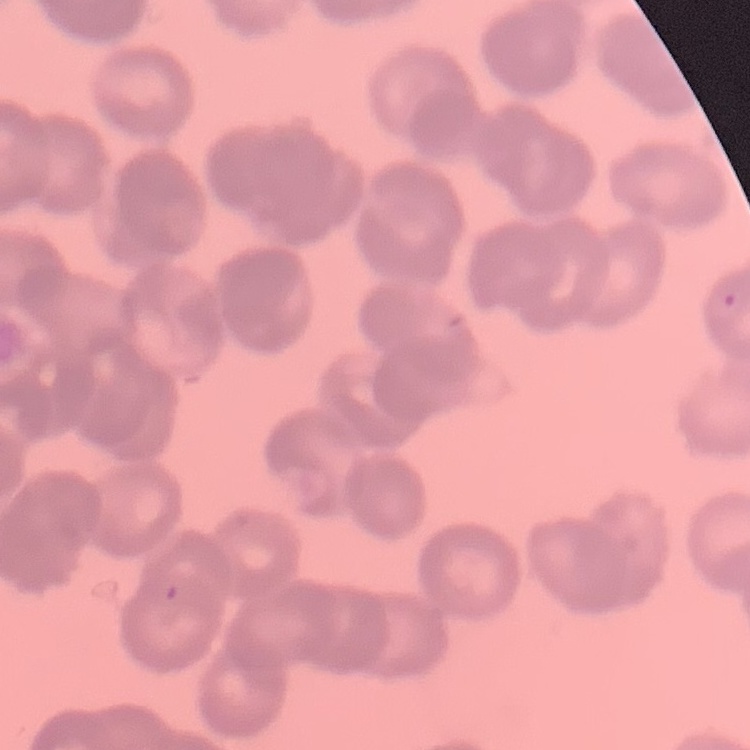
red blood cell morphology = rouleaux formation
preparation = thin blood smear
image type = one tile cut from a larger photomicrograph
stain = Field's or Giemsa